Name the blood parasite species.
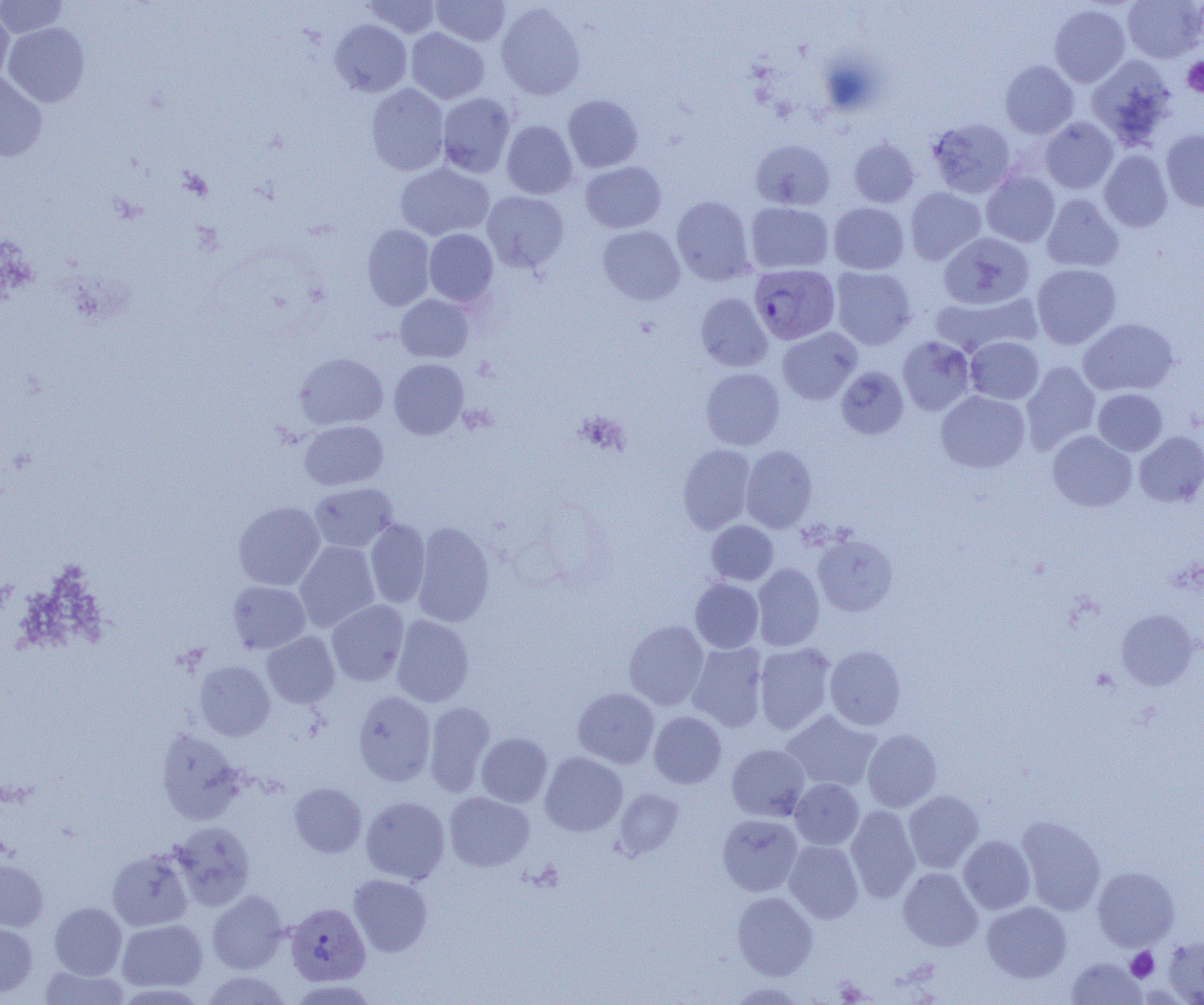
Plasmodium vivax.

Approximate bounding boxes as [x1, y1, x2, y2] in pixels. Uninfected red blood cell locations: [0, 0, 67, 38], [360, 0, 442, 38], [431, 0, 510, 46], [1122, 0, 1203, 62], [495, 2, 586, 100], [1049, 3, 1131, 87], [0, 7, 14, 85], [330, 19, 411, 97], [3, 22, 90, 107], [406, 28, 489, 104], [1086, 55, 1177, 149], [1000, 60, 1079, 139], [0, 72, 47, 161], [366, 84, 449, 175], [437, 93, 516, 177], [563, 95, 643, 172], [1039, 117, 1118, 194], [927, 118, 1016, 198], [501, 120, 577, 199], [1161, 130, 1204, 211], [849, 138, 920, 208], [750, 139, 834, 210], [1099, 149, 1173, 232], [580, 161, 666, 233], [395, 162, 494, 241], [981, 171, 1060, 247], [905, 187, 986, 265], [482, 191, 568, 272], [1041, 194, 1124, 272], [671, 195, 755, 286], [745, 201, 833, 274], [829, 202, 909, 275], [362, 224, 435, 310], [598, 225, 685, 305], [424, 229, 498, 306], [938, 232, 1035, 309], [1032, 263, 1121, 349], [830, 267, 917, 350], [932, 291, 1042, 357], [695, 292, 773, 372], [395, 294, 473, 362], [1078, 318, 1179, 396], [778, 327, 861, 404], [965, 336, 1044, 404], [897, 337, 976, 415], [294, 352, 387, 431], [389, 358, 469, 439], [1021, 361, 1101, 453], [836, 366, 909, 439], [701, 367, 785, 450], [1093, 389, 1168, 456], [936, 390, 1030, 473], [300, 420, 387, 490], [1047, 430, 1137, 512], [1134, 431, 1204, 507], [677, 444, 756, 534], [741, 445, 817, 532], [309, 483, 398, 553], [234, 501, 325, 591], [365, 519, 430, 608], [706, 520, 778, 585], [412, 521, 495, 627], [812, 534, 898, 616], [294, 540, 380, 632], [752, 563, 825, 651], [690, 578, 764, 653], [228, 581, 311, 653], [327, 600, 409, 686], [1115, 609, 1198, 690], [391, 615, 474, 707], [624, 620, 709, 709], [262, 632, 340, 709], [687, 642, 768, 732], [754, 642, 836, 735], [824, 645, 906, 730], [195, 661, 274, 740], [573, 688, 660, 768], [353, 691, 436, 785], [424, 701, 496, 796], [781, 710, 882, 792], [649, 711, 726, 788], [156, 729, 246, 824], [862, 729, 942, 812], [476, 732, 552, 807], [726, 743, 810, 821], [539, 752, 627, 836], [790, 779, 864, 850], [289, 782, 366, 857], [614, 788, 684, 858], [903, 790, 983, 873], [444, 792, 534, 871], [360, 796, 450, 885], [846, 805, 921, 903], [718, 814, 803, 896], [1016, 816, 1106, 915], [170, 821, 255, 910], [958, 835, 1035, 914], [784, 840, 863, 923], [107, 849, 193, 932], [0, 859, 48, 931], [1093, 866, 1180, 951], [898, 867, 982, 951], [348, 873, 432, 957], [207, 890, 289, 973], [732, 891, 817, 979], [982, 901, 1072, 982], [49, 902, 127, 979], [117, 919, 207, 993], [0, 921, 37, 997], [1164, 936, 1204, 1004], [1066, 957, 1146, 1004], [39, 966, 130, 1004], [201, 971, 294, 1005], [724, 982, 808, 1004]. Plasmodium vivax-infected red blood cell locations: [749, 264, 840, 345], [285, 902, 370, 986]. Platelet locations: [1182, 57, 1204, 97], [1126, 947, 1159, 982], [835, 979, 869, 1003]. Single field of view. Thin blood film. 1000x magnification. Image is 1204×1005 pixels. Optical microscopy.